Report the malaria status of this cell.
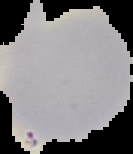

Uninfected.

preparation = thin blood smear
image type = cell region segmented out of the field of view; surrounding area masked to black
image size = 133×154 pixels